State which parasite is depicted.
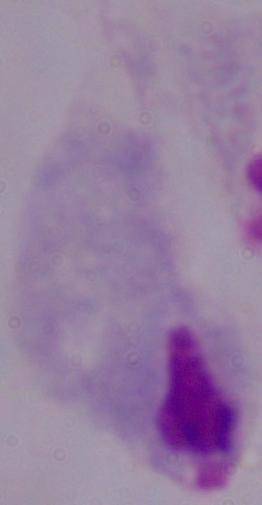

This is a trichomonad.

Summary:
  - Modality: photomicrograph
  - Magnification: 1000x